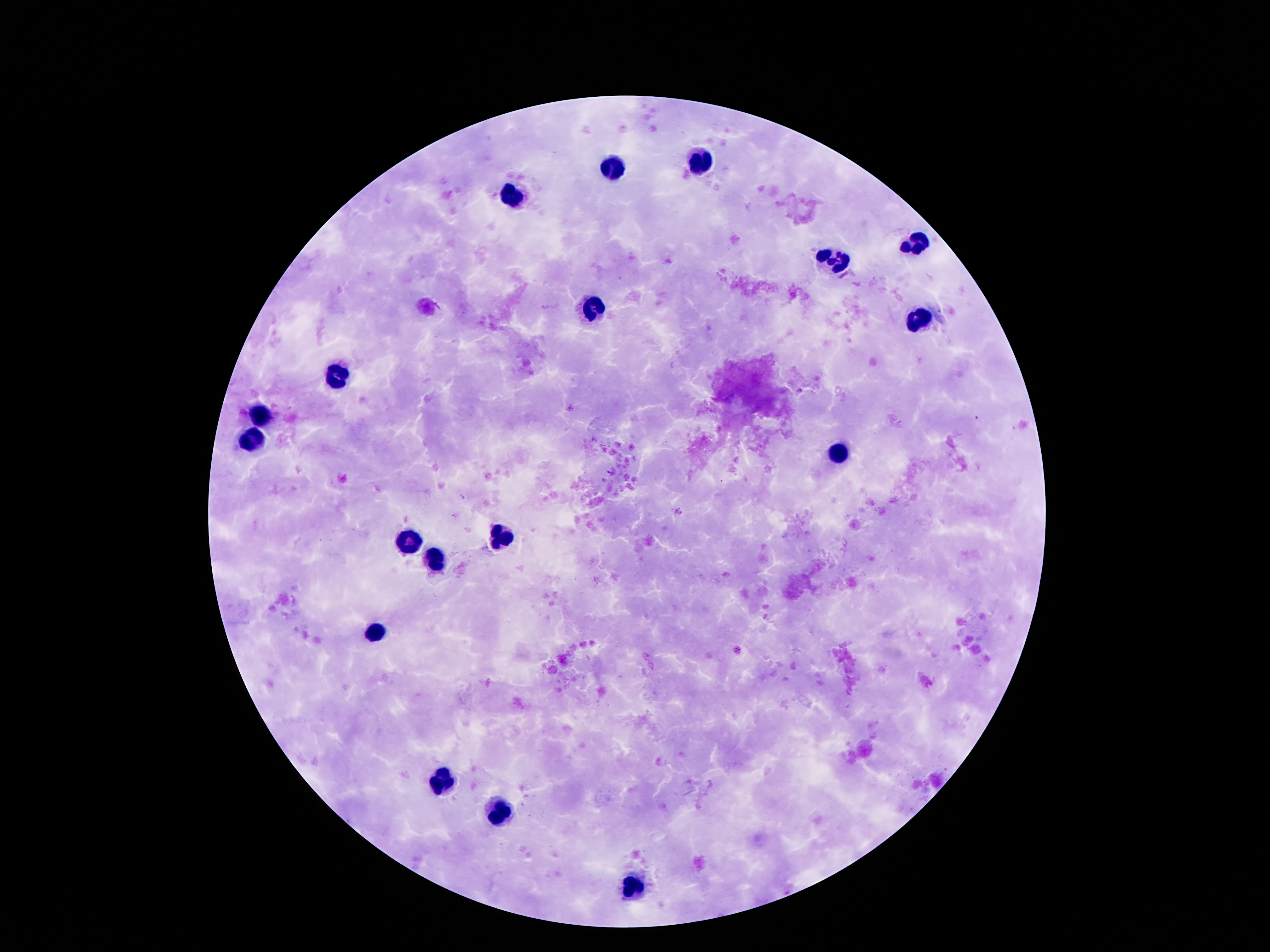
{
  "patient_malaria_status": "negative",
  "capture": "smartphone camera through the microscope eyepiece",
  "stain": "Giemsa",
  "field_of_view": "single",
  "magnification": "100x",
  "image_size": "1270×952 pixels",
  "preparation": "thick blood smear",
  "leukocyte_locations": "approximate centers as (x, y) in pixels: (700, 159), (612, 167), (513, 197), (918, 246), (833, 262), (592, 308), (916, 322), (338, 376), (259, 419), (252, 440), (839, 455), (501, 535), (408, 539), (437, 559), (377, 631), (439, 780), (497, 813), (635, 886)"
}